Locate every leukocyte (white blood cell).
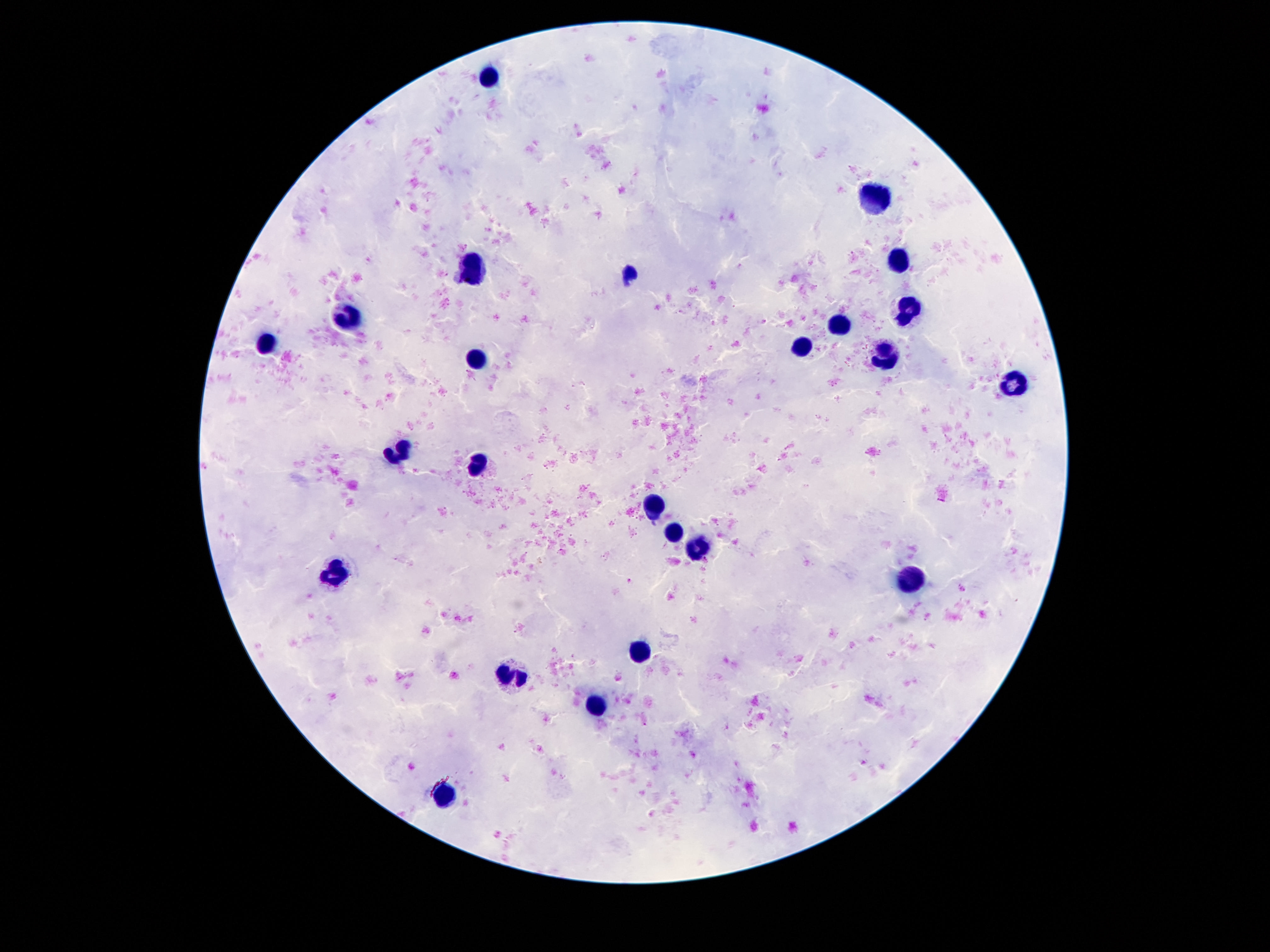
Approximate object centers, in pixels from the top-left corner.
Leukocytes: (x=491, y=76), (x=877, y=196), (x=899, y=257), (x=471, y=264), (x=907, y=310), (x=351, y=315), (x=835, y=324), (x=265, y=340), (x=801, y=346), (x=885, y=354), (x=475, y=358), (x=1013, y=383), (x=399, y=450), (x=477, y=464), (x=653, y=503), (x=671, y=530), (x=699, y=549), (x=331, y=574), (x=913, y=581), (x=637, y=654), (x=509, y=674), (x=597, y=708), (x=445, y=793).

Thick blood smear. Giemsa stain. Patient malaria status: negative. Image is 1270×952 pixels. Photographed through the microscope eyepiece with a smartphone camera. Single field of view. 100x magnification.